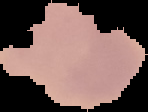
Segmented cell region on a black background. From a thin blood smear. Image is 148×112 pixels. Result: no malaria parasites detected.